Locate every blood parasite and identify its species.
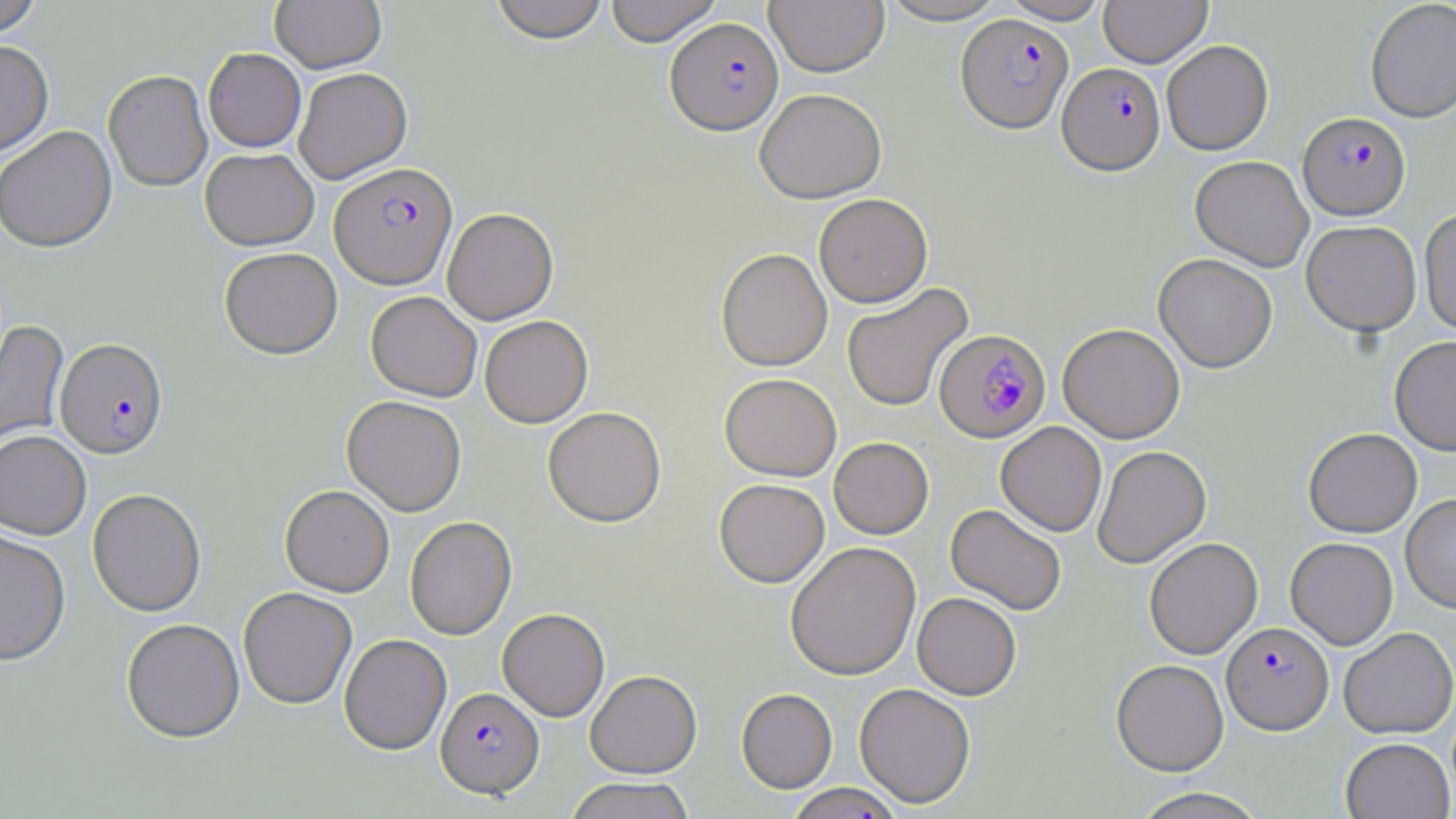

Approximate bounding boxes as (x1,y1)-(x2,y2) corner pairs in pixels.
Plasmodium falciparum-infected red blood cells: (957,14)-(1073,132), (665,18)-(783,136), (1058,63)-(1165,175), (1298,112)-(1410,220), (330,164)-(457,290), (935,329)-(1050,443), (56,338)-(169,459), (1222,621)-(1333,735), (436,687)-(544,798).
No Plasmodium ovale, Plasmodium malariae, Plasmodium vivax, Babesia divergens, or Trypanosoma brucei observed.

Summary:
  - Uninfected red blood cell locations: (489,0)-(610,45), (604,0)-(724,46), (766,0)-(889,77), (876,0)-(1012,25), (998,0)-(1113,24), (1099,0)-(1212,67), (1365,0)-(1456,122), (0,1)-(43,39), (270,1)-(386,73), (1162,40)-(1273,155), (0,41)-(53,157), (203,48)-(306,152), (294,68)-(412,184), (103,71)-(212,193), (755,89)-(886,203), (0,127)-(117,253), (200,148)-(319,251), (1190,155)-(1314,272), (814,194)-(933,308), (1419,206)-(1456,336), (442,209)-(558,325), (1301,221)-(1421,336), (219,248)-(342,360), (716,248)-(832,372), (1153,253)-(1277,372), (841,283)-(973,412), (366,292)-(482,402), (480,315)-(593,428), (0,320)-(69,450), (1058,323)-(1185,442), (1390,336)-(1456,455), (720,373)-(841,481), (342,396)-(466,516), (543,407)-(666,528), (996,422)-(1107,537), (1303,428)-(1422,537), (0,431)-(91,540), (829,437)-(933,539), (1093,445)-(1211,568), (714,478)-(830,588), (280,486)-(394,597), (88,490)-(207,617), (1400,493)-(1456,612), (945,504)-(1066,615), (405,517)-(517,640), (0,530)-(71,668), (1144,537)-(1262,659), (1285,537)-(1397,649), (785,542)-(921,680), (239,588)-(357,709), (912,592)-(1021,700), (497,609)-(609,722), (121,620)-(245,743), (1339,627)-(1455,738), (339,634)-(451,755), (1111,659)-(1229,776), (586,670)-(702,778), (854,683)-(976,808), (736,688)-(837,793), (1340,737)-(1454,819), (565,777)-(695,819), (785,783)-(905,819), (1128,787)-(1271,819)
  - Slide-level diagnosis: Plasmodium falciparum
  - Preparation: thin blood film
  - Modality: optical microscopy
  - Magnification: 1000x
  - Image size: 1456×819 pixels
  - Field of view: one of a larger specimen
  - Stain: May-Grünwald-Giemsa